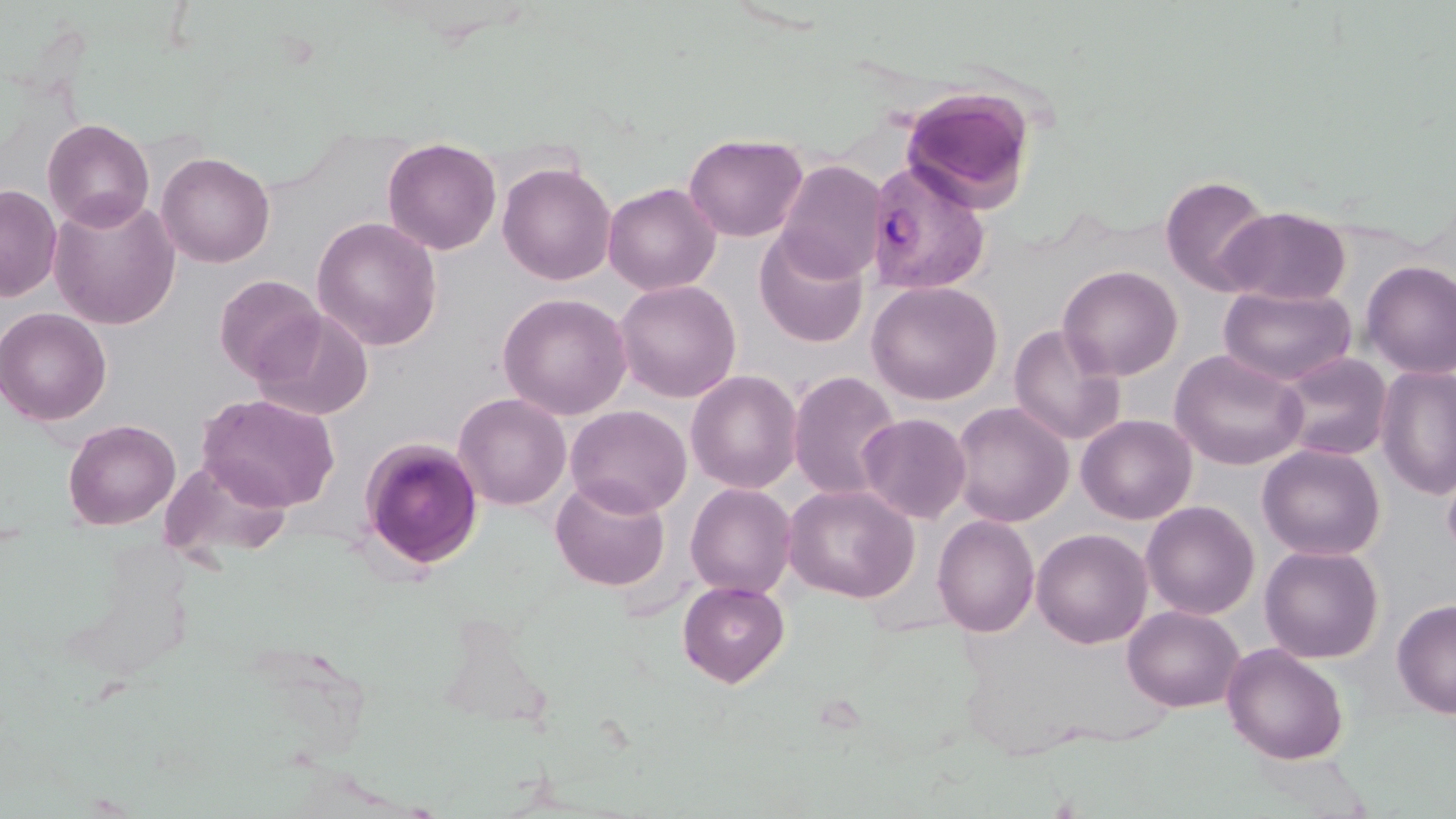

Approximate bounding boxes as named x1/y1/x2/y2 corners in pixels. Uninfected red blood cell locations: (x1=899, y1=86, x2=1037, y2=211), (x1=42, y1=117, x2=155, y2=231), (x1=684, y1=133, x2=808, y2=242), (x1=382, y1=138, x2=501, y2=255), (x1=156, y1=151, x2=275, y2=267), (x1=775, y1=160, x2=886, y2=282), (x1=497, y1=161, x2=616, y2=285), (x1=345, y1=166, x2=482, y2=317), (x1=1160, y1=174, x2=1273, y2=295), (x1=603, y1=182, x2=721, y2=295), (x1=0, y1=185, x2=61, y2=301), (x1=48, y1=193, x2=181, y2=329), (x1=1220, y1=206, x2=1352, y2=305), (x1=311, y1=217, x2=443, y2=351), (x1=754, y1=230, x2=869, y2=347), (x1=1360, y1=261, x2=1456, y2=379), (x1=1058, y1=264, x2=1183, y2=381), (x1=214, y1=274, x2=325, y2=383), (x1=614, y1=279, x2=741, y2=402), (x1=866, y1=280, x2=1003, y2=405), (x1=1219, y1=286, x2=1357, y2=386), (x1=498, y1=293, x2=632, y2=420), (x1=0, y1=307, x2=111, y2=425), (x1=250, y1=308, x2=374, y2=421), (x1=1009, y1=323, x2=1127, y2=447), (x1=1170, y1=350, x2=1309, y2=470), (x1=1275, y1=352, x2=1391, y2=461), (x1=1375, y1=365, x2=1456, y2=500), (x1=685, y1=370, x2=803, y2=493), (x1=788, y1=370, x2=902, y2=502), (x1=198, y1=393, x2=340, y2=511), (x1=453, y1=393, x2=571, y2=510), (x1=950, y1=402, x2=1074, y2=527), (x1=566, y1=405, x2=692, y2=517), (x1=857, y1=413, x2=971, y2=524), (x1=1076, y1=414, x2=1197, y2=525), (x1=63, y1=419, x2=180, y2=529), (x1=358, y1=437, x2=484, y2=570), (x1=1257, y1=444, x2=1386, y2=561), (x1=160, y1=456, x2=294, y2=567), (x1=1440, y1=456, x2=1456, y2=563), (x1=551, y1=477, x2=670, y2=591), (x1=685, y1=483, x2=797, y2=599), (x1=783, y1=483, x2=919, y2=602), (x1=1140, y1=501, x2=1259, y2=619), (x1=933, y1=515, x2=1040, y2=637), (x1=1031, y1=528, x2=1152, y2=649), (x1=1260, y1=545, x2=1384, y2=663), (x1=677, y1=580, x2=790, y2=687), (x1=1392, y1=598, x2=1456, y2=719), (x1=1122, y1=605, x2=1244, y2=712), (x1=1222, y1=643, x2=1349, y2=764). Plasmodium vivax-infected red blood cell locations: (x1=866, y1=159, x2=992, y2=295). Slide-level diagnosis: Plasmodium vivax. Image is 1456×819 pixels. Thin blood film. Light microscopy. May-Grünwald-Giemsa-stained preparation. One field of a larger specimen. 1000x magnification.